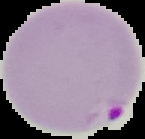
preparation = thin blood smear
result = Plasmodium parasites detected
image size = 145×139 pixels
image type = segmented cell region with the area outside set to black